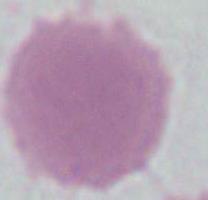

Summary:
  - Identification: red blood cell
  - Magnification: 1000x
  - Modality: photomicrograph